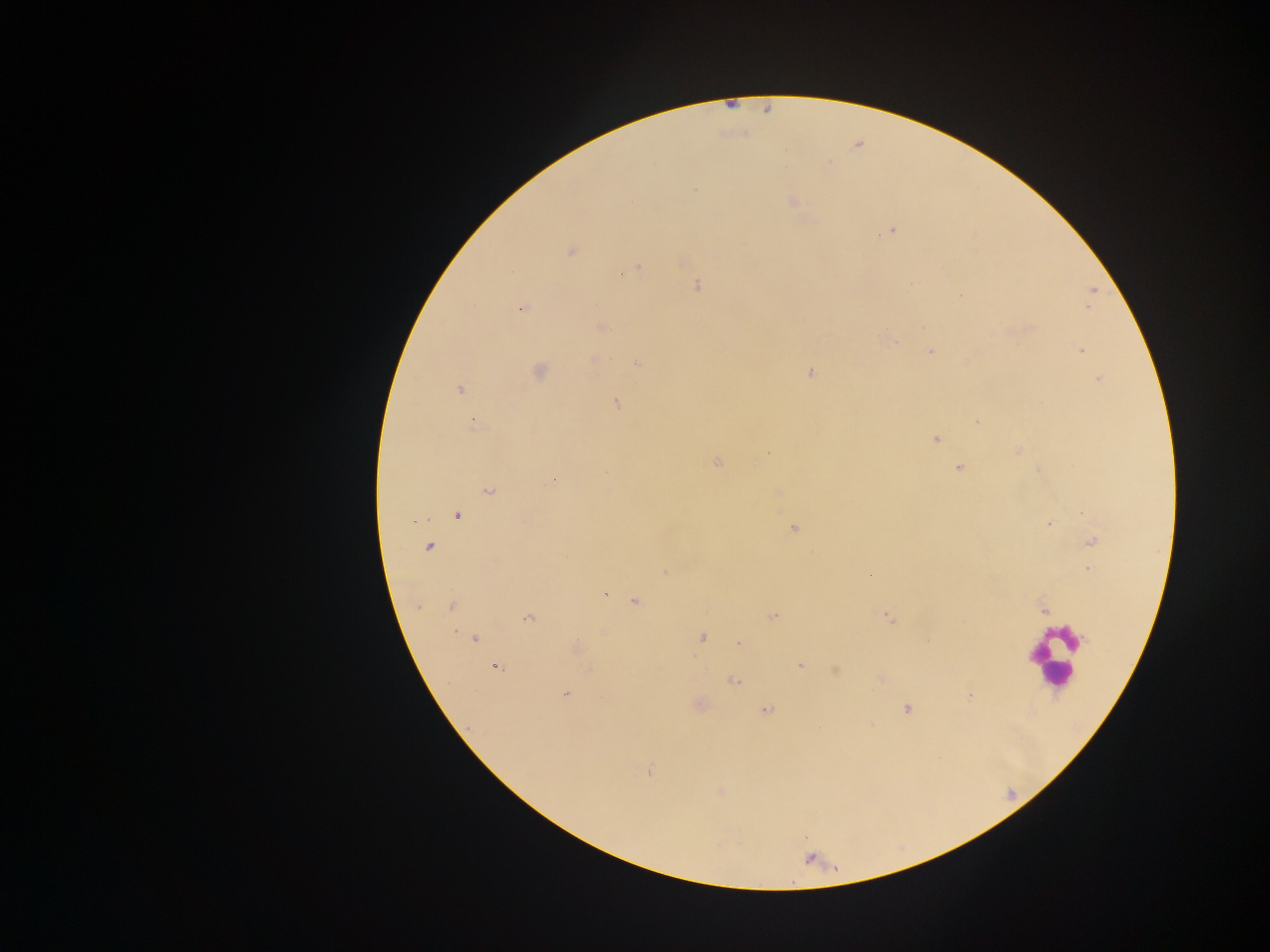

Approximate centers as [x, y] in pixels. Malaria parasite locations: [695, 189], [791, 201], [888, 232], [570, 251], [637, 269], [621, 275], [698, 286], [1093, 290], [1090, 302], [1087, 307], [522, 309], [601, 326], [894, 341], [1082, 350], [931, 351], [593, 360], [637, 364], [539, 371], [811, 372], [1098, 380], [459, 389], [616, 402], [976, 421], [473, 425], [936, 438], [1018, 450], [768, 452], [717, 462], [958, 468], [553, 479], [488, 491], [457, 516], [1048, 524], [793, 528], [1092, 542], [428, 547], [1088, 569], [665, 572], [605, 595], [635, 601], [417, 607], [452, 607], [1044, 609], [773, 616], [886, 617], [528, 618], [702, 638], [474, 639], [738, 644], [576, 646], [801, 666], [496, 668], [735, 682], [565, 695], [970, 696], [906, 708], [766, 710], [649, 772]. Leukocyte locations: [1053, 655]. Thick blood film. Image is 1270×952 pixels. One field of view. Sample from Ghana. Mobile-phone photograph taken through the microscope.